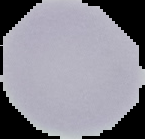

image type = segmented cell region with the area outside set to black
preparation = thin blood smear
image size = 145×139 pixels
result = no Plasmodium parasites seen